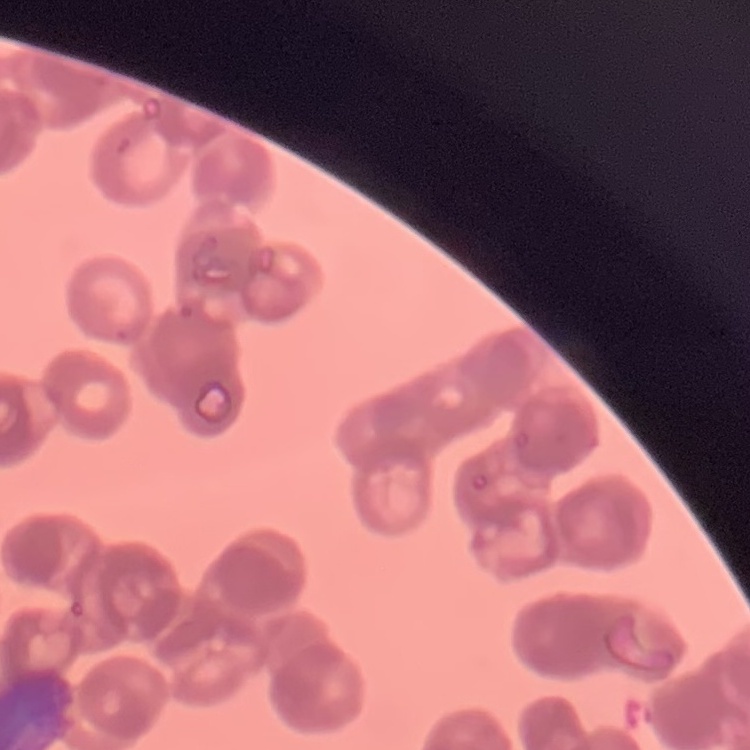
red blood cell morphology = rouleaux formation
image type = one tile cut from a larger photomicrograph
preparation = thin peripheral smear
stain = Field's or Giemsa